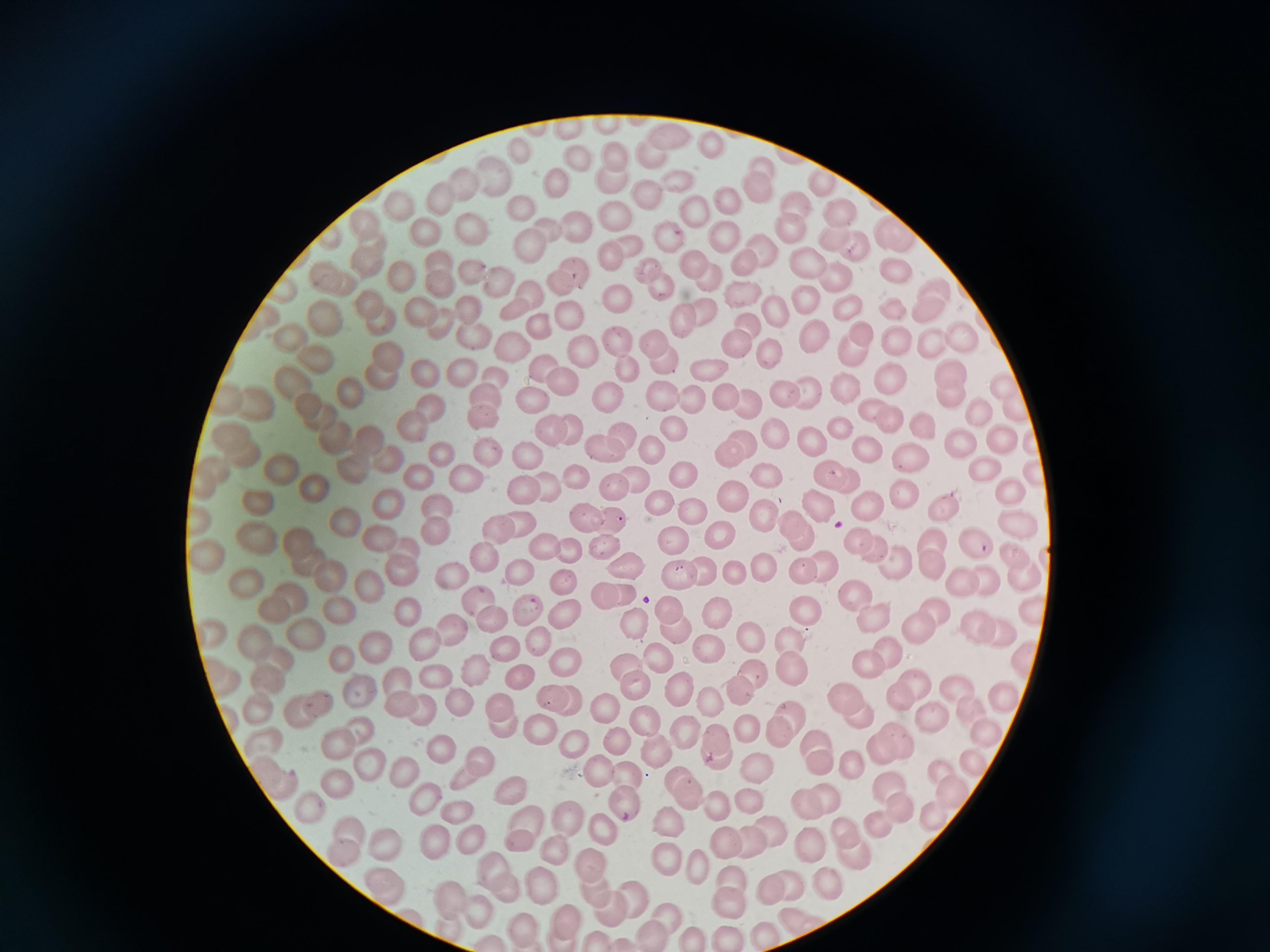 Approximate centers as [x, y] in pixels. Cell locations: [605, 121], [569, 122], [671, 137], [711, 143], [521, 151], [618, 155], [649, 155], [578, 160], [761, 164], [491, 173], [557, 177], [820, 179], [678, 180], [463, 182], [612, 183], [759, 189], [646, 198], [443, 199], [730, 199], [793, 204], [694, 208], [835, 208], [400, 209], [521, 211], [614, 216], [367, 221], [793, 226], [574, 228], [472, 229], [546, 230], [421, 231], [666, 235], [727, 235], [897, 238], [829, 239], [627, 246], [852, 247], [528, 248], [762, 252], [439, 257], [613, 257], [366, 261], [691, 262], [811, 266], [647, 267], [743, 267], [472, 268], [577, 270], [890, 274], [832, 276], [333, 279], [498, 280], [402, 281], [708, 281], [443, 285], [280, 286], [558, 288], [662, 289], [934, 291], [798, 299], [619, 301], [373, 305], [845, 305], [422, 308], [892, 308], [518, 309], [466, 312], [929, 312], [706, 313], [328, 314], [768, 314], [566, 316], [681, 318], [380, 322], [745, 325], [542, 327], [861, 331], [474, 333], [961, 337], [655, 339], [808, 339], [298, 340], [620, 340], [898, 342], [928, 342], [736, 346], [512, 348], [576, 353], [852, 355], [322, 357], [762, 358], [388, 359], [664, 362], [539, 367], [709, 369], [628, 370], [464, 371], [427, 375], [379, 376], [889, 376], [299, 381], [500, 381], [563, 384], [842, 384], [1001, 386], [350, 389], [663, 391], [783, 393], [809, 393], [488, 395], [948, 395], [609, 396], [691, 397], [721, 397], [534, 398], [256, 400], [746, 402], [309, 405], [868, 407], [1019, 408], [429, 409], [979, 409], [325, 417], [486, 418], [890, 420], [918, 423], [410, 426], [673, 427], [838, 427], [775, 430], [549, 431], [573, 431], [998, 433], [233, 434], [620, 435], [371, 438], [335, 439], [807, 439], [1031, 440], [961, 441], [743, 442], [866, 444], [600, 446], [646, 448], [443, 452], [488, 452], [242, 455], [525, 455], [727, 455], [909, 456], [384, 457], [277, 469], [979, 469], [214, 470], [352, 470], [1028, 471], [418, 472], [830, 473], [681, 475], [765, 475], [464, 476], [576, 478], [850, 478], [633, 479], [199, 483], [616, 485], [544, 487], [308, 489], [523, 490], [1012, 491], [902, 494], [729, 496], [658, 499], [822, 503], [385, 504], [864, 504], [435, 505], [261, 506], [691, 507], [947, 510], [346, 518], [199, 519], [584, 519], [614, 519], [762, 519], [792, 520], [1017, 521], [522, 522], [720, 530], [499, 531], [436, 534], [378, 535], [298, 536], [857, 538], [254, 539], [670, 540], [799, 541], [973, 541], [605, 542], [932, 543], [568, 548], [871, 548], [207, 550], [406, 551], [481, 554], [1012, 556], [308, 559], [625, 560], [894, 561], [763, 562], [399, 567], [821, 567], [930, 567], [519, 569], [736, 570], [801, 570], [697, 571], [678, 572], [448, 574], [1020, 575], [327, 576], [984, 579], [565, 581], [246, 582], [368, 585], [959, 585], [627, 589], [293, 591], [854, 592], [604, 593], [478, 599], [273, 605], [670, 606], [333, 607], [933, 607], [523, 609], [410, 610], [807, 611], [561, 613], [718, 613], [1031, 615], [490, 618], [874, 618], [632, 623], [978, 625], [669, 626], [449, 628], [209, 630], [917, 630], [994, 634], [303, 636], [750, 637], [257, 640], [538, 642], [793, 643], [415, 646], [368, 647], [505, 648], [713, 648], [884, 651], [340, 659], [1026, 659], [278, 660], [658, 661], [559, 663], [624, 663], [864, 663], [751, 670], [788, 670], [473, 672], [518, 673], [219, 674], [267, 675], [435, 675], [912, 676], [636, 683], [682, 688], [958, 689], [738, 692], [1005, 694], [552, 696], [357, 697], [900, 697], [572, 700], [844, 700], [710, 701], [313, 702], [401, 703], [459, 704], [608, 705], [260, 707], [501, 707], [419, 708], [296, 710], [788, 711], [930, 714], [972, 714], [229, 716], [860, 719], [501, 724], [648, 724], [743, 726], [359, 729], [539, 729], [777, 730], [682, 732], [987, 734], [815, 738], [893, 738], [614, 740], [338, 741], [574, 741], [263, 743], [717, 743], [878, 743], [443, 747], [654, 757], [476, 761], [849, 763], [818, 764], [970, 765], [367, 766], [755, 766], [597, 769], [941, 771], [399, 773], [270, 776], [629, 776], [465, 778], [677, 779], [335, 786], [510, 787], [888, 788], [953, 792], [823, 796], [687, 797], [808, 801], [747, 802], [625, 804], [304, 806], [714, 806], [902, 807], [933, 813], [452, 814], [520, 822], [567, 822], [668, 823], [879, 824], [602, 828], [845, 829], [771, 831], [347, 833], [465, 838], [433, 840], [748, 841], [517, 842], [725, 842], [389, 844], [812, 844], [549, 849], [851, 849], [339, 853], [666, 855], [489, 864], [591, 864], [697, 866], [729, 878], [380, 880], [827, 881], [543, 882], [790, 882], [769, 888], [500, 889], [593, 893], [449, 899], [630, 901], [729, 903], [477, 911], [611, 911], [662, 915], [799, 919], [561, 924], [518, 930], [765, 935], [651, 937], [690, 937], [724, 938], [598, 940]. Acquired by smartphone through the microscope eyepiece. Giemsa stain. Single field of view. Image is 1270×952 pixels. Thin blood film.